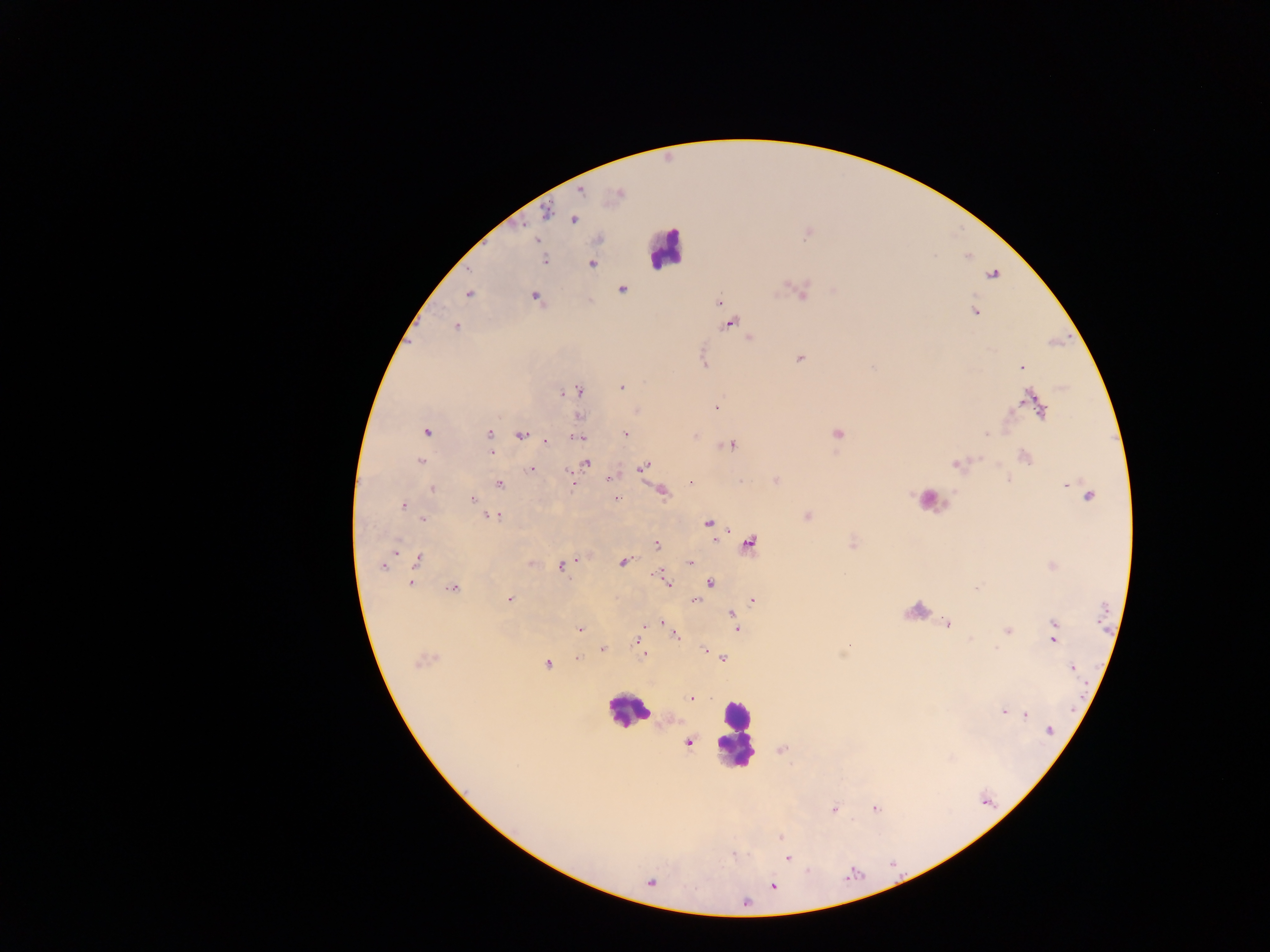

Approximate centers as [x, y] in pixels.
Summary:
  - Leukocyte locations: [665, 248], [930, 496], [627, 712], [735, 733]
  - Malaria parasite locations: [582, 192], [619, 193], [546, 212], [574, 220], [544, 259], [592, 263], [993, 274], [623, 289], [802, 292], [468, 294], [535, 297], [719, 301], [975, 311], [730, 323], [456, 326], [749, 338], [799, 358], [1022, 367], [621, 387], [578, 391], [563, 393], [1032, 401], [715, 406], [1039, 409], [426, 431], [490, 434], [626, 434], [838, 434], [986, 435], [521, 436], [578, 437], [546, 441], [731, 445], [491, 452], [1025, 457], [421, 461], [586, 462], [956, 464], [643, 467], [531, 469], [610, 479], [572, 480], [777, 480], [691, 482], [499, 484], [1068, 487], [432, 489], [663, 492], [1089, 496], [616, 498], [472, 500], [403, 506], [807, 515], [493, 516], [423, 519], [709, 523], [750, 544], [657, 545], [418, 560], [623, 562], [690, 562], [532, 563], [382, 566], [561, 566], [659, 575], [667, 583], [711, 583], [411, 584], [976, 587], [452, 588], [508, 601], [695, 601], [753, 601], [732, 615], [735, 622], [662, 623], [948, 624], [737, 628], [1055, 628], [579, 629], [1007, 631], [675, 635], [1054, 637], [637, 641], [849, 645], [996, 649], [602, 650], [704, 651], [642, 652], [578, 657], [724, 658], [423, 661], [548, 664], [1072, 668], [691, 698], [1003, 712], [1026, 715], [1050, 731], [689, 743], [875, 808], [833, 810], [782, 838], [733, 855], [787, 858], [808, 871], [773, 886], [745, 901]
  - Country: Ghana
  - Preparation: thick blood film
  - Field of view: single
  - Image size: 1270×952 pixels
  - Capture: mobile-phone photograph through a microscope